Locate every uninfected red blood cell.
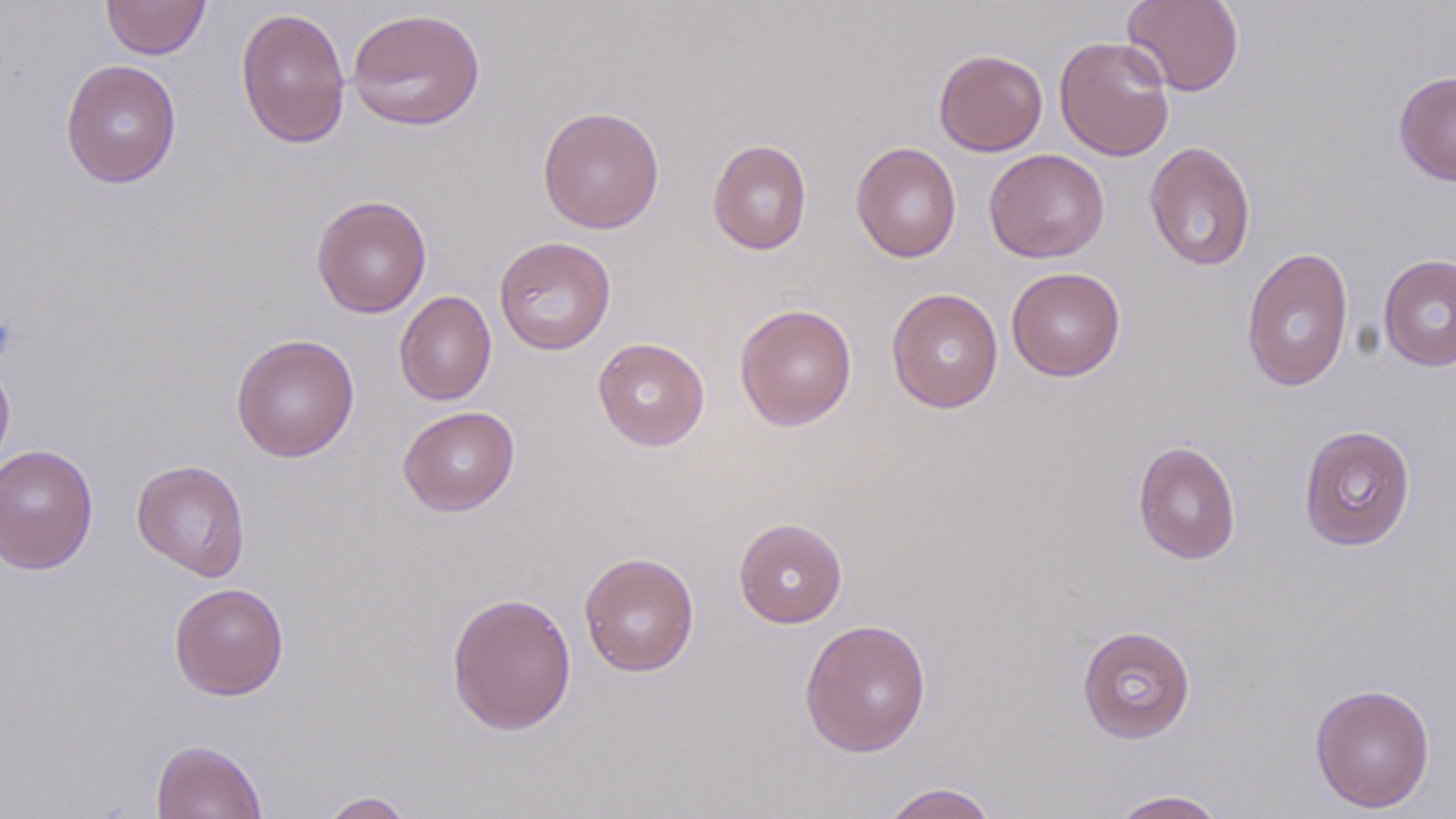

Approximate bounding boxes as (x1, y1, x2, y2) in pixels.
Uninfected red blood cells: (100, 0, 211, 60), (1122, 0, 1244, 96), (235, 7, 351, 149), (346, 7, 486, 132), (1054, 35, 1175, 161), (934, 49, 1048, 156), (60, 59, 182, 188), (1394, 70, 1456, 185), (537, 105, 665, 234), (708, 138, 812, 255), (1144, 141, 1257, 271), (851, 142, 961, 262), (983, 148, 1109, 263), (311, 195, 432, 318), (494, 236, 616, 355), (1241, 247, 1354, 393), (1378, 254, 1456, 371), (1006, 266, 1126, 381), (886, 287, 1004, 413), (394, 290, 497, 406), (734, 303, 857, 431), (231, 333, 360, 462), (592, 337, 710, 451), (0, 357, 15, 477), (397, 406, 520, 516), (1298, 424, 1416, 551), (1133, 440, 1241, 564), (0, 444, 99, 575), (131, 459, 251, 581), (734, 518, 847, 628), (579, 552, 700, 677), (168, 582, 289, 700), (446, 591, 577, 735), (799, 618, 932, 757), (1078, 625, 1196, 743), (1309, 682, 1435, 813), (151, 739, 267, 819), (880, 782, 1000, 819), (1109, 789, 1228, 818), (316, 791, 416, 818).

Summary:
  - Slide-level diagnosis: no evidence of blood parasites
  - Field of view: single
  - Image size: 1456×819 pixels
  - Preparation: thin blood film
  - Magnification: 1000x
  - Stain: May-Grünwald-Giemsa
  - Modality: light microscopy